Report the malaria status of this cell.
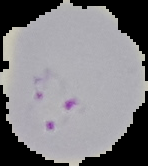
Parasitized.

Segmented cell region on a black background. Image is 148×166 pixels. From a thin blood film.